Give the position of every Plasmodium parasite visible.
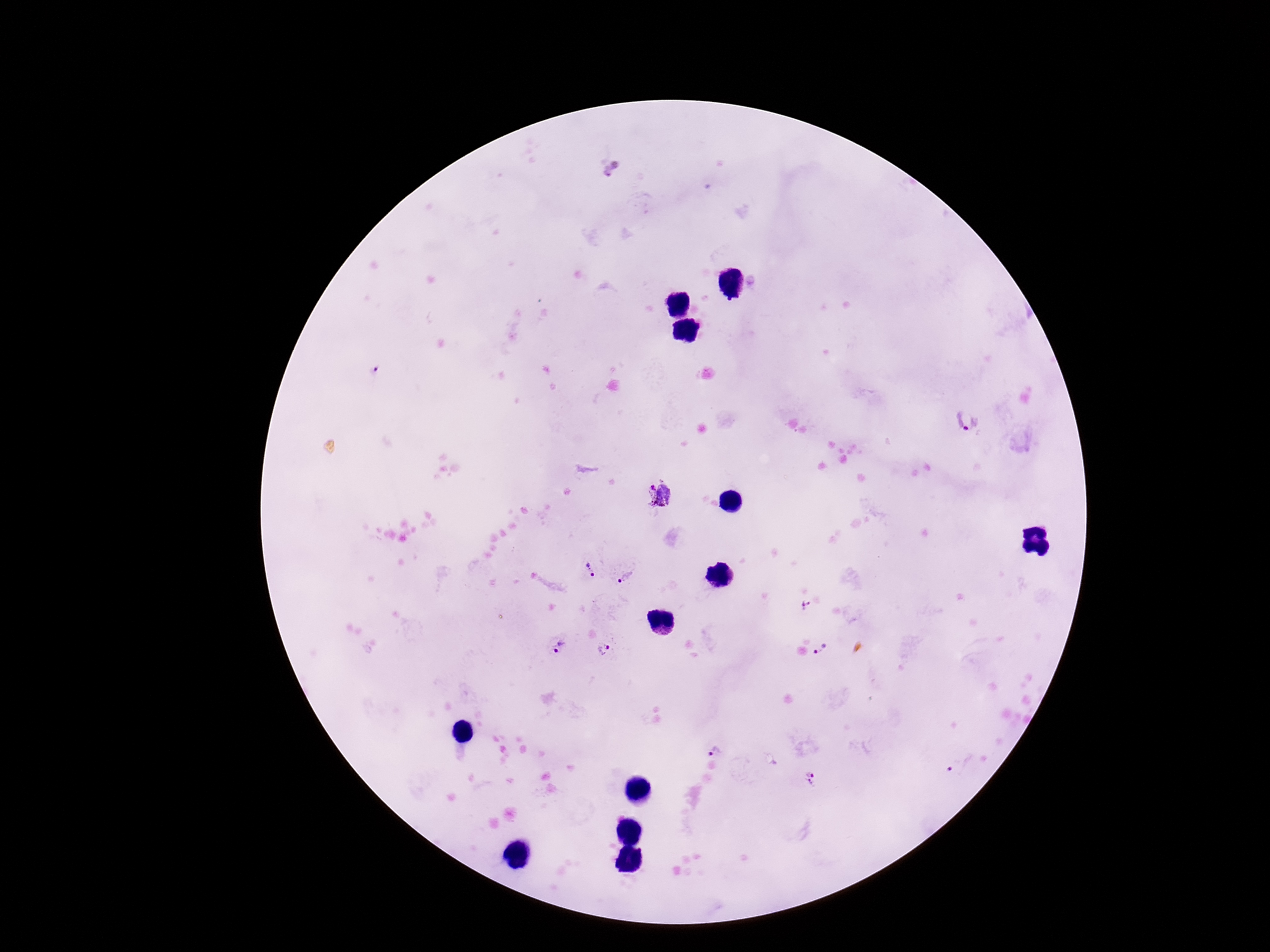

Approximate centers as {x, y} in pixels.
Plasmodium parasites: {613, 170}, {376, 371}, {966, 423}, {662, 495}, {590, 570}, {626, 578}, {804, 605}, {560, 647}, {603, 649}, {820, 649}, {716, 753}, {957, 768}, {812, 779}.

image size = 1270×952 pixels
stain = Giemsa
patient malaria status = infected
magnification = 100x
capture = smartphone camera through the microscope eyepiece
preparation = thick blood smear
field of view = one from this slide